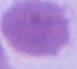
modality = photomicrograph
identification = erythrocyte
magnification = 1000x